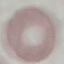
Summary:
  - Result: no malaria parasites seen
  - Stain: Giemsa
  - Capture: smartphone through the microscope eyepiece
  - Image type: cell patch, automatically extracted from a larger field of view and resized to 64 × 64 pixels
  - Preparation: thin blood smear